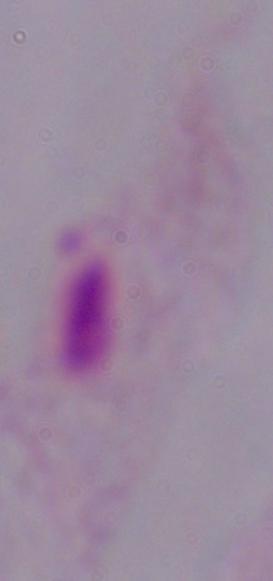
Summary:
  - Modality: photomicrograph
  - Identification: trichomonad
  - Magnification: 1000x